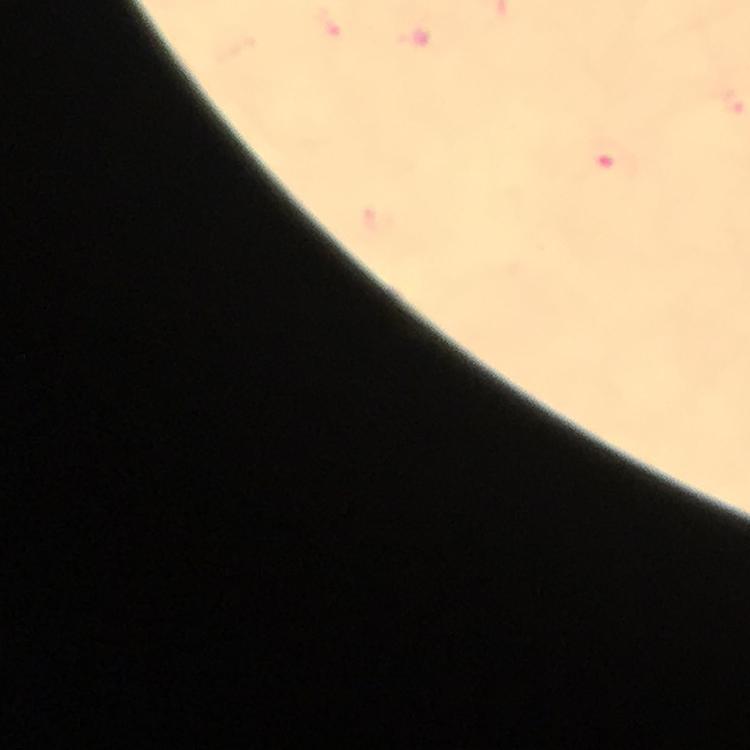

malaria parasite locations = approximate object centers, in pixels from the top-left corner: (x=607, y=157)
preparation = thick blood film
magnification = 100x
cropped from = a single field of view
stain = Giemsa
image size = 750×750 pixels
context = from a malaria diagnostic workup
immersion oil = applied
capture = smartphone camera through the microscope